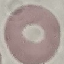
Result: negative for malaria parasites. Automatically extracted cell patch, resized to 64 × 64 pixels. Thin blood smear. Photographed with a smartphone camera at the microscope eyepiece. Giemsa-stained preparation.